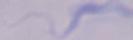
Photomicrograph. A trypanosome is shown. Captured at 1000x magnification.